State which cell type is depicted.
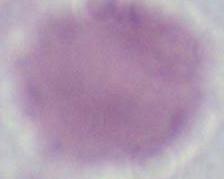
An erythrocyte.

Summary:
  - Modality: micrograph
  - Magnification: 1000x